Assess this cell for malaria.
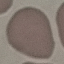
It is uninfected.

capture = smartphone through the microscope eyepiece
image type = cell patch, automatically extracted from a larger field of view and resized to 64 × 64 pixels
preparation = thin smear
stain = Giemsa